Find the cells and give the type of each one.
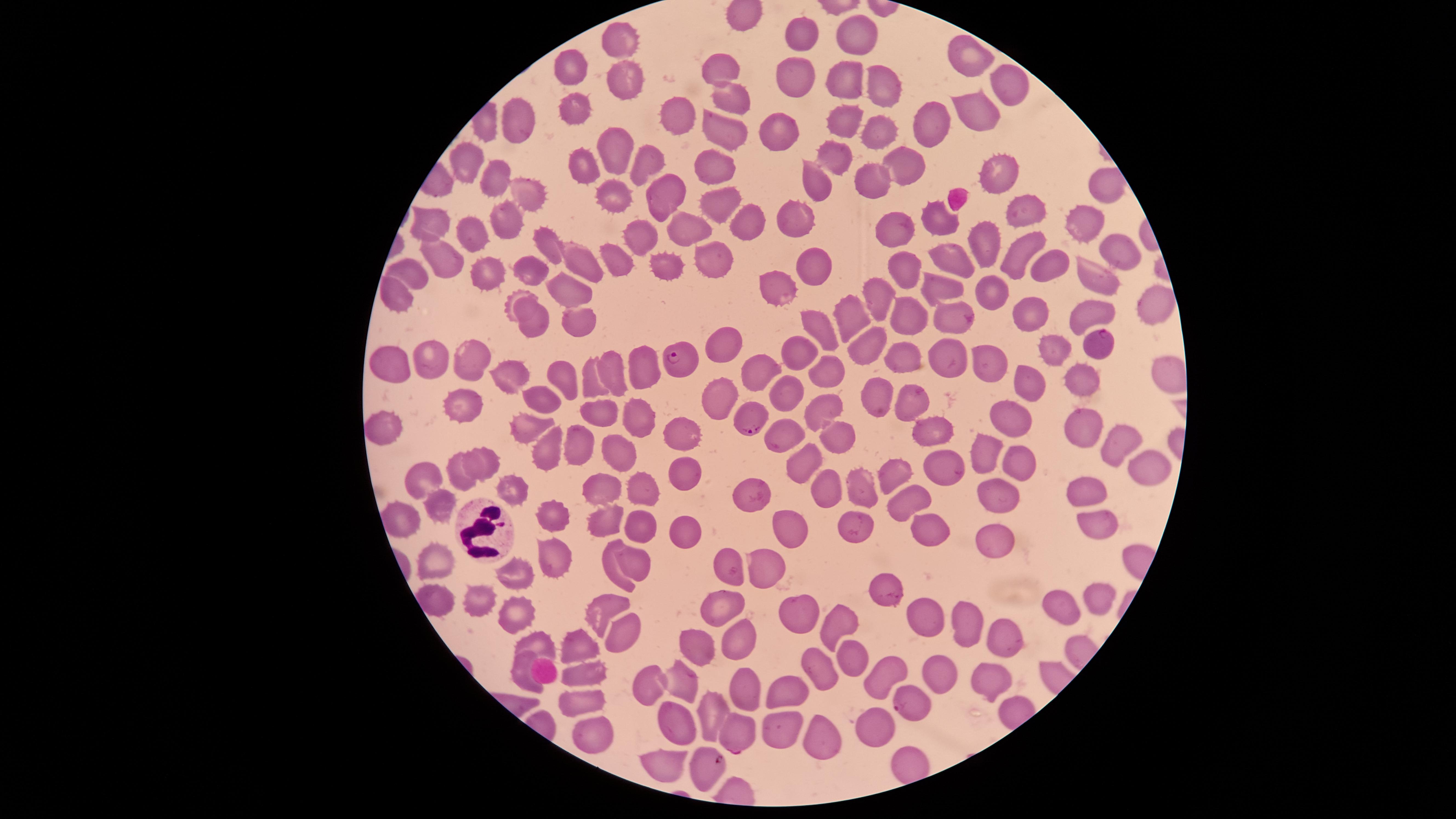

Approximate marker points, in pixels from the top-left corner.
Parasitized RBCs: (x=1095, y=340), (x=677, y=357), (x=747, y=412), (x=912, y=702), (x=736, y=734), (x=705, y=767).
Uninfected RBCs: (x=798, y=35), (x=854, y=36), (x=617, y=41), (x=969, y=53), (x=568, y=67), (x=720, y=69), (x=800, y=80), (x=883, y=80), (x=1008, y=80), (x=622, y=84), (x=846, y=91), (x=732, y=99), (x=576, y=108), (x=980, y=109), (x=673, y=117), (x=931, y=123), (x=514, y=125), (x=847, y=125), (x=783, y=134), (x=884, y=134), (x=723, y=137), (x=613, y=151), (x=836, y=154), (x=643, y=160), (x=469, y=162), (x=584, y=164), (x=906, y=164), (x=719, y=172), (x=1001, y=172), (x=492, y=178), (x=874, y=180), (x=1107, y=180), (x=823, y=183), (x=522, y=191), (x=665, y=193), (x=609, y=194), (x=719, y=204), (x=1026, y=207), (x=1079, y=216), (x=801, y=217), (x=935, y=218), (x=505, y=219), (x=430, y=221), (x=747, y=228), (x=687, y=230), (x=896, y=231), (x=475, y=234), (x=637, y=238), (x=990, y=242), (x=548, y=245), (x=1013, y=251), (x=1124, y=251), (x=711, y=254), (x=950, y=255), (x=614, y=257), (x=438, y=259), (x=577, y=263), (x=1048, y=263), (x=907, y=266), (x=813, y=267), (x=667, y=268), (x=411, y=270), (x=481, y=271), (x=531, y=276), (x=1101, y=277), (x=880, y=284), (x=773, y=286), (x=939, y=286), (x=395, y=291), (x=994, y=291), (x=565, y=292), (x=517, y=300), (x=1152, y=303), (x=1091, y=307), (x=1030, y=313), (x=910, y=315), (x=949, y=315), (x=851, y=316), (x=536, y=321), (x=582, y=321), (x=827, y=324), (x=725, y=343), (x=865, y=343), (x=1052, y=345), (x=952, y=354), (x=906, y=358), (x=804, y=360), (x=470, y=361), (x=427, y=363), (x=643, y=363), (x=996, y=363), (x=394, y=364), (x=1178, y=368), (x=613, y=373), (x=760, y=373), (x=832, y=373), (x=564, y=376), (x=511, y=377), (x=590, y=379), (x=1030, y=381), (x=1084, y=381), (x=788, y=390), (x=716, y=397), (x=911, y=397), (x=542, y=400), (x=873, y=400), (x=819, y=406), (x=465, y=407), (x=1009, y=415), (x=591, y=417), (x=636, y=417), (x=1081, y=423), (x=522, y=425), (x=381, y=430), (x=932, y=430), (x=681, y=435), (x=830, y=438), (x=782, y=439), (x=574, y=443), (x=1109, y=444), (x=547, y=447), (x=617, y=454), (x=982, y=456), (x=1016, y=456), (x=483, y=459), (x=798, y=462), (x=945, y=465), (x=1141, y=467), (x=682, y=470), (x=458, y=473), (x=899, y=473), (x=429, y=475), (x=508, y=487), (x=635, y=487), (x=819, y=487), (x=861, y=488), (x=601, y=489), (x=1084, y=490), (x=750, y=494), (x=990, y=497), (x=908, y=503), (x=437, y=506), (x=547, y=512), (x=398, y=515), (x=603, y=515), (x=642, y=521), (x=852, y=521), (x=1091, y=521), (x=790, y=522), (x=682, y=528), (x=926, y=531), (x=991, y=539), (x=554, y=558), (x=433, y=559), (x=633, y=561), (x=762, y=562), (x=609, y=563), (x=512, y=569), (x=730, y=570), (x=877, y=587), (x=433, y=595), (x=1093, y=597), (x=483, y=599), (x=515, y=607), (x=603, y=608), (x=719, y=608), (x=1057, y=608), (x=921, y=613), (x=794, y=615), (x=964, y=616), (x=838, y=622), (x=618, y=629), (x=537, y=636), (x=742, y=640), (x=1009, y=641), (x=699, y=644), (x=572, y=645), (x=846, y=658), (x=937, y=665), (x=521, y=668), (x=583, y=671), (x=817, y=674), (x=989, y=675), (x=685, y=677), (x=876, y=678), (x=742, y=681), (x=650, y=684), (x=783, y=688), (x=580, y=700), (x=709, y=709), (x=679, y=719), (x=778, y=727), (x=871, y=727), (x=594, y=733), (x=828, y=740), (x=669, y=765).
WBCs: (x=485, y=530).

Summary:
  - Capture: smartphone photograph through the microscope eyepiece
  - Preparation: thin blood film
  - Species: Plasmodium falciparum
  - Visible region: circular
  - Image size: 1456×819 pixels
  - Field of view: single
  - Stain: Giemsa